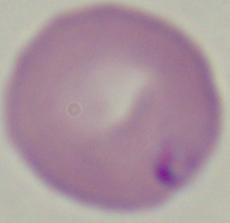
magnification = 1000x
modality = photomicrograph
identification = Babesia